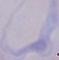

1000x magnification. A trypanosome is shown. Micrograph.